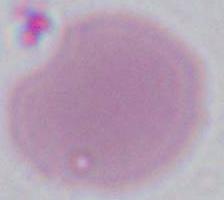
magnification = 1000x
identification = red blood cell
modality = photomicrograph